Name the parasite shown.
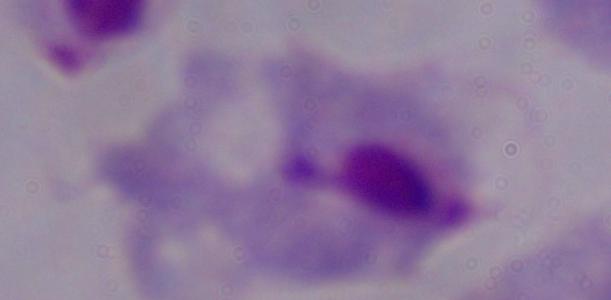

A trichomonad.

{
  "magnification": "1000x",
  "modality": "photomicrograph"
}